Report the malaria status of this cell.
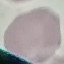

Uninfected.

Summary:
  - Capture: smartphone through the microscope eyepiece
  - Stain: Giemsa
  - Preparation: thin blood film
  - Image type: cell patch, automatically extracted from a larger field of view and resized to 64 × 64 pixels